Outline each blood parasite and name the species.
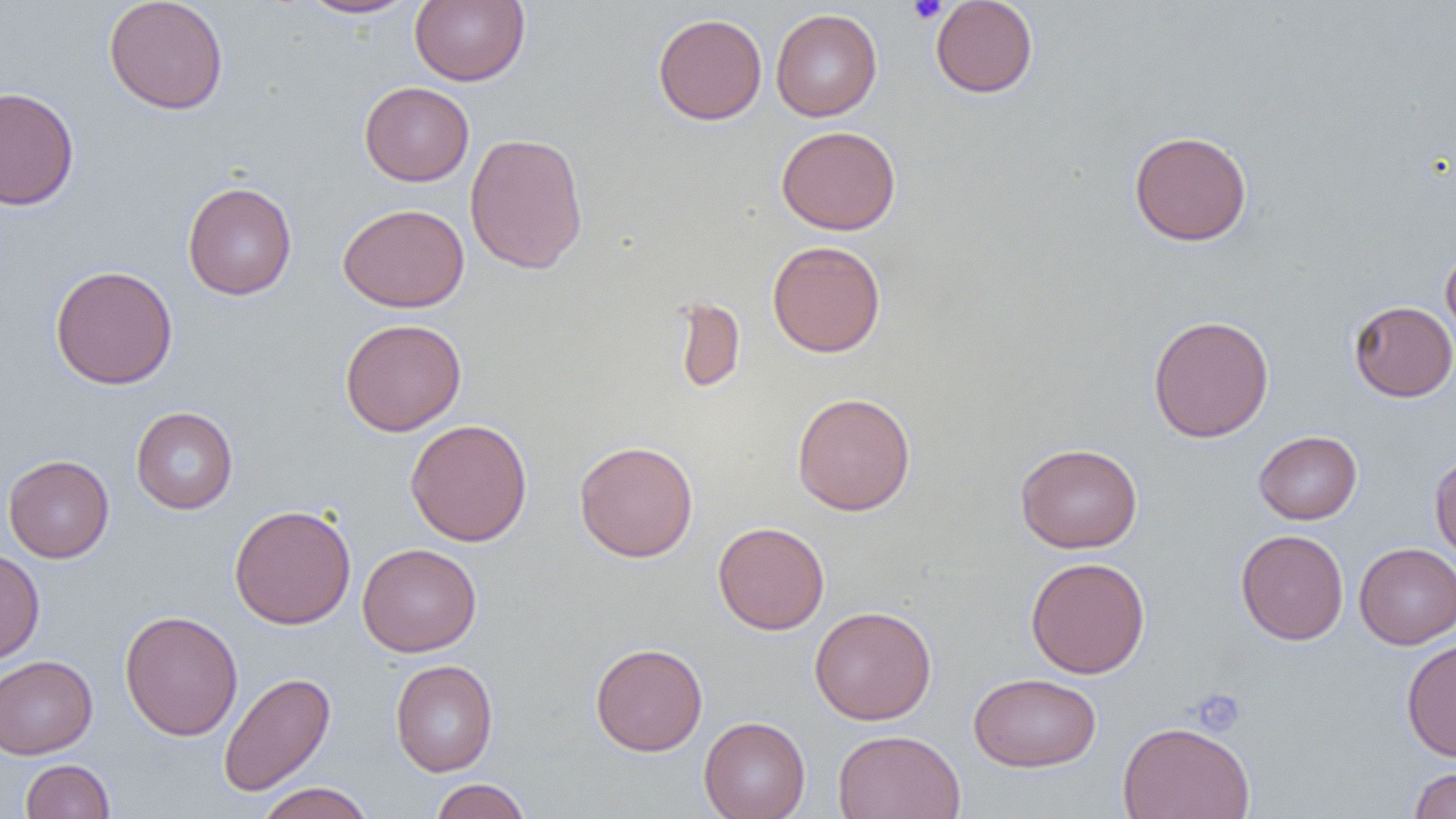
No blood parasites observed.

Approximate bounding boxes as named x1/y1/x2/y2 corners in pixels. Uninfected red blood cell locations: (x1=103, y1=0, x2=229, y2=115), (x1=297, y1=0, x2=419, y2=19), (x1=410, y1=0, x2=530, y2=86), (x1=930, y1=0, x2=1039, y2=98), (x1=770, y1=8, x2=882, y2=121), (x1=652, y1=12, x2=767, y2=125), (x1=359, y1=81, x2=474, y2=186), (x1=0, y1=86, x2=80, y2=211), (x1=776, y1=125, x2=901, y2=235), (x1=1129, y1=130, x2=1253, y2=246), (x1=464, y1=132, x2=589, y2=274), (x1=182, y1=181, x2=297, y2=300), (x1=338, y1=203, x2=469, y2=313), (x1=767, y1=241, x2=886, y2=358), (x1=1441, y1=245, x2=1456, y2=343), (x1=50, y1=265, x2=178, y2=390), (x1=672, y1=295, x2=746, y2=394), (x1=1349, y1=300, x2=1456, y2=402), (x1=1148, y1=314, x2=1274, y2=442), (x1=340, y1=318, x2=466, y2=436), (x1=792, y1=391, x2=916, y2=516), (x1=131, y1=407, x2=238, y2=514), (x1=405, y1=419, x2=533, y2=547), (x1=1253, y1=431, x2=1362, y2=524), (x1=574, y1=440, x2=699, y2=562), (x1=1015, y1=442, x2=1143, y2=553), (x1=1430, y1=451, x2=1456, y2=565), (x1=3, y1=454, x2=114, y2=563), (x1=229, y1=504, x2=356, y2=630), (x1=713, y1=521, x2=830, y2=635), (x1=1236, y1=529, x2=1349, y2=645), (x1=357, y1=542, x2=482, y2=657), (x1=1354, y1=543, x2=1456, y2=649), (x1=0, y1=549, x2=45, y2=665), (x1=1025, y1=557, x2=1150, y2=679), (x1=810, y1=605, x2=937, y2=725), (x1=120, y1=609, x2=243, y2=741), (x1=1401, y1=638, x2=1456, y2=762), (x1=591, y1=643, x2=708, y2=755), (x1=0, y1=656, x2=98, y2=759), (x1=390, y1=659, x2=498, y2=776), (x1=218, y1=671, x2=335, y2=797), (x1=968, y1=672, x2=1101, y2=772), (x1=698, y1=716, x2=811, y2=819), (x1=1117, y1=720, x2=1256, y2=819), (x1=833, y1=729, x2=966, y2=819), (x1=20, y1=759, x2=115, y2=818), (x1=1407, y1=767, x2=1456, y2=819), (x1=429, y1=778, x2=532, y2=819), (x1=255, y1=782, x2=376, y2=819). Platelet locations: (x1=907, y1=0, x2=948, y2=24), (x1=1190, y1=688, x2=1246, y2=737). Slide-level diagnosis: negative for blood parasites. One field of a larger specimen. Thin blood film. Optical microscopy. Captured at 1000x magnification. Image is 1456×819 pixels.